State which parasite is depicted.
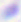

Toxoplasma gondii.

modality = micrograph
magnification = 400x